Report the malaria status of this cell.
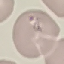
It is parasitized.

{
  "stain": "Giemsa",
  "image_type": "automatically extracted cell patch, resized to 64 × 64 pixels",
  "capture": "smartphone through the microscope eyepiece",
  "preparation": "thin blood smear"
}